Describe the morphology of the erythrocytes.
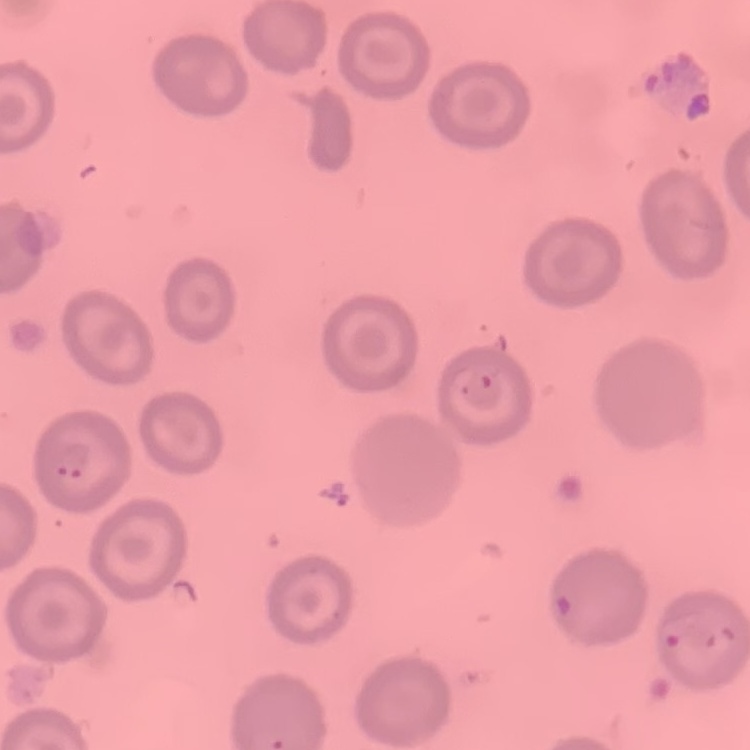

They show no rouleaux formation.

image type = square crop of a larger photomicrograph
preparation = thin blood smear
stain = Field's or Giemsa